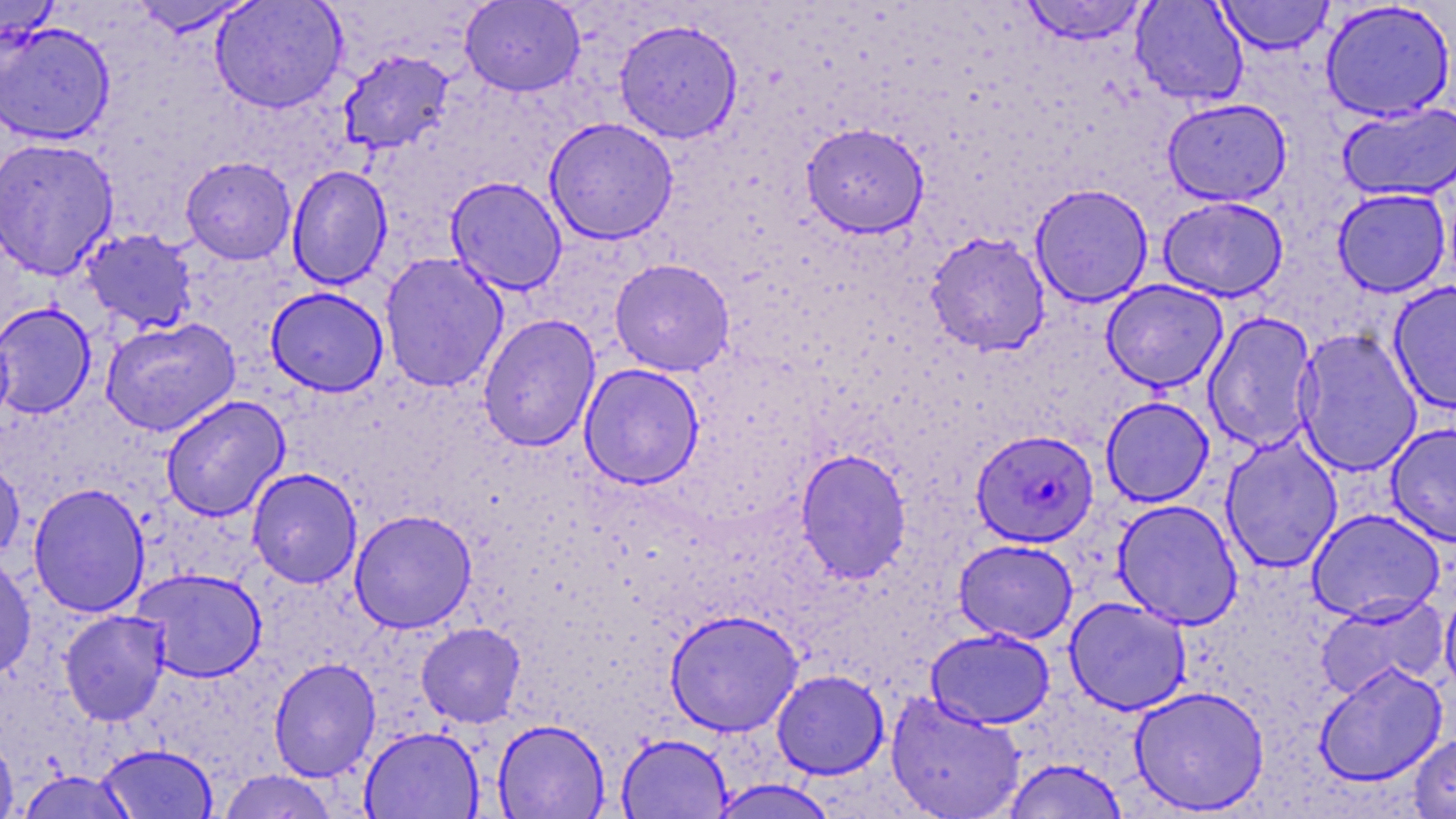
Approximate bounding boxes as [x1, y1, x2, y2] in pixels. Plasmodium falciparum-infected red blood cell locations: [971, 429, 1099, 548]. Uninfected red blood cell locations: [210, 0, 347, 113], [459, 0, 586, 97], [1019, 0, 1150, 45], [1130, 0, 1249, 106], [1215, 0, 1334, 54], [0, 1, 62, 46], [127, 1, 259, 37], [1320, 1, 1456, 122], [614, 18, 743, 144], [0, 22, 116, 145], [337, 50, 455, 155], [1162, 97, 1292, 206], [1337, 101, 1456, 202], [543, 117, 679, 245], [801, 123, 929, 238], [0, 137, 120, 280], [180, 156, 296, 265], [286, 164, 393, 290], [445, 176, 568, 295], [1030, 183, 1154, 307], [1332, 188, 1452, 297], [1158, 196, 1288, 302], [79, 228, 199, 334], [925, 231, 1051, 356], [380, 252, 508, 393], [609, 258, 735, 376], [1101, 279, 1228, 392], [1388, 281, 1456, 414], [266, 287, 389, 397], [0, 302, 97, 419], [1203, 311, 1318, 454], [478, 314, 600, 451], [100, 317, 240, 436], [1294, 328, 1423, 477], [579, 363, 705, 489], [160, 395, 290, 522], [1101, 396, 1215, 507], [1386, 422, 1456, 547], [1221, 435, 1343, 573], [795, 449, 912, 583], [0, 455, 25, 561], [247, 468, 362, 588], [27, 483, 150, 618], [1113, 499, 1244, 630], [1307, 508, 1445, 623], [349, 509, 477, 633], [953, 539, 1078, 644], [0, 555, 37, 680], [132, 568, 267, 683], [1439, 583, 1456, 703], [1314, 594, 1449, 701], [1064, 596, 1192, 715], [664, 609, 804, 736], [59, 610, 171, 726], [416, 622, 526, 728], [925, 628, 1055, 729], [268, 658, 381, 782], [1313, 661, 1448, 787], [771, 669, 889, 779], [1129, 685, 1270, 815], [885, 691, 1026, 818], [492, 719, 610, 818], [359, 725, 484, 818], [0, 733, 18, 818], [616, 733, 732, 818], [1408, 733, 1456, 818], [96, 743, 219, 819], [1002, 759, 1128, 819], [217, 769, 340, 818], [711, 779, 839, 818]. Slide-level diagnosis: Plasmodium falciparum. Optical microscopy. 1000x magnification. Thin blood smear. May-Grünwald-Giemsa stain. Single field of view. Image is 1456×819 pixels.